Name the parasite shown.
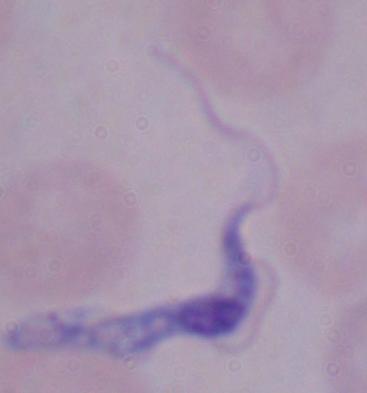

This is a trypanosome.

modality: micrograph
magnification: 1000x